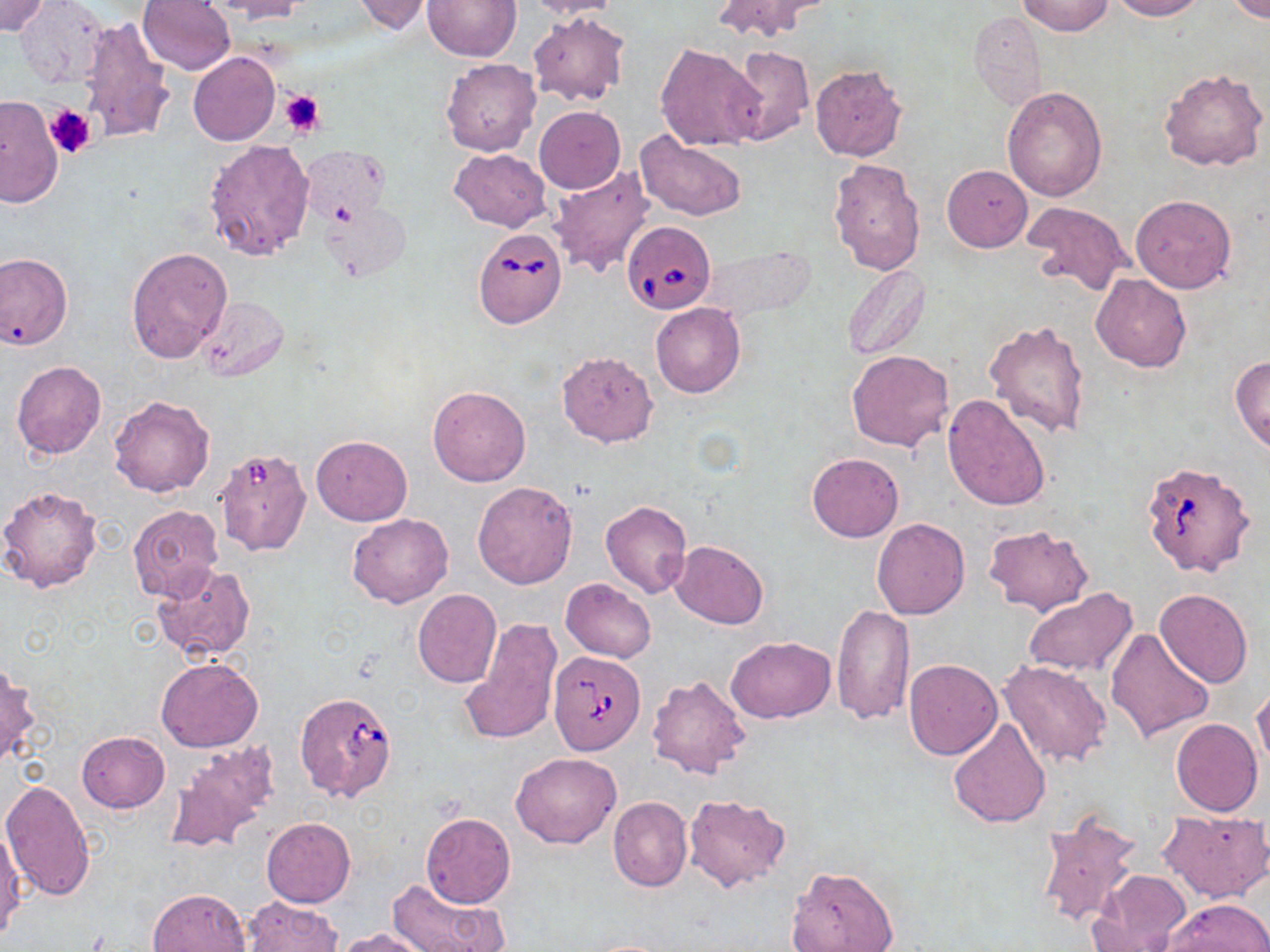

Summary:
  - Coordinate format: approximate bounding boxes as (x1,y1)-(x2,y2) corner pairs in pixels
  - Uninfected red blood cell locations: (0,0)-(49,36), (136,0)-(236,75), (207,0)-(309,22), (349,0)-(437,35), (423,0)-(520,61), (520,0)-(622,19), (711,0)-(828,41), (1107,0)-(1204,21), (1226,0)-(1269,23), (1017,1)-(1113,36), (16,4)-(107,89), (526,10)-(632,107), (968,10)-(1046,108), (77,15)-(178,145), (655,43)-(764,151), (727,44)-(814,145), (188,52)-(280,146), (440,58)-(541,156), (810,65)-(907,161), (1159,69)-(1268,173), (1001,87)-(1108,201), (0,96)-(64,207), (535,107)-(624,192), (633,132)-(748,221), (204,138)-(316,262), (299,147)-(390,227), (450,148)-(551,232), (828,156)-(927,277), (551,164)-(656,280), (942,165)-(1032,252), (1130,195)-(1236,293), (323,196)-(411,279), (1021,201)-(1130,299), (126,248)-(233,363), (0,252)-(73,350), (842,264)-(930,361), (1090,274)-(1190,372), (195,296)-(288,381), (650,303)-(745,397), (985,320)-(1091,437), (846,350)-(954,451), (557,352)-(658,447), (1229,354)-(1270,452), (12,360)-(106,458), (427,386)-(531,487), (944,394)-(1050,512), (108,395)-(215,498), (312,434)-(412,525), (806,453)-(903,542), (472,481)-(579,589), (0,486)-(102,593), (601,501)-(692,599), (127,505)-(223,602), (348,513)-(453,608), (871,518)-(969,619), (983,524)-(1093,615), (671,540)-(768,628), (151,564)-(254,662), (560,578)-(655,662), (412,588)-(502,688), (1022,588)-(1138,679), (1155,588)-(1251,688), (831,604)-(914,725), (460,617)-(562,747), (1105,628)-(1215,743), (725,635)-(835,722), (156,657)-(264,752), (904,659)-(1001,760), (999,660)-(1112,768), (0,664)-(39,767), (646,674)-(752,781), (1251,685)-(1270,780), (946,715)-(1051,828), (1171,718)-(1263,816), (76,732)-(170,813), (165,739)-(281,855), (511,751)-(621,848), (1,780)-(96,902), (684,795)-(791,891), (607,796)-(691,892), (1035,809)-(1143,931), (1159,810)-(1270,901), (420,813)-(516,909), (262,817)-(355,907), (0,826)-(25,940), (789,866)-(899,952), (1089,868)-(1193,951), (385,878)-(508,952), (148,888)-(251,952), (243,897)-(342,952), (1159,899)-(1269,952), (335,928)-(436,952)
  - Platelet locations: (280,88)-(327,135), (44,105)-(96,159)
  - Babesia divergens-infected red blood cell locations: (621,221)-(716,314), (473,225)-(565,327), (1142,459)-(1256,576), (549,653)-(644,755), (294,691)-(397,802)
  - Slide-level diagnosis: Babesia divergens
  - Magnification: 1000x
  - Stain: May-Grünwald-Giemsa
  - Modality: light microscopy
  - Preparation: thin blood smear
  - Image size: 1270×952 pixels
  - Field of view: single